Outline each blood parasite and name the species.
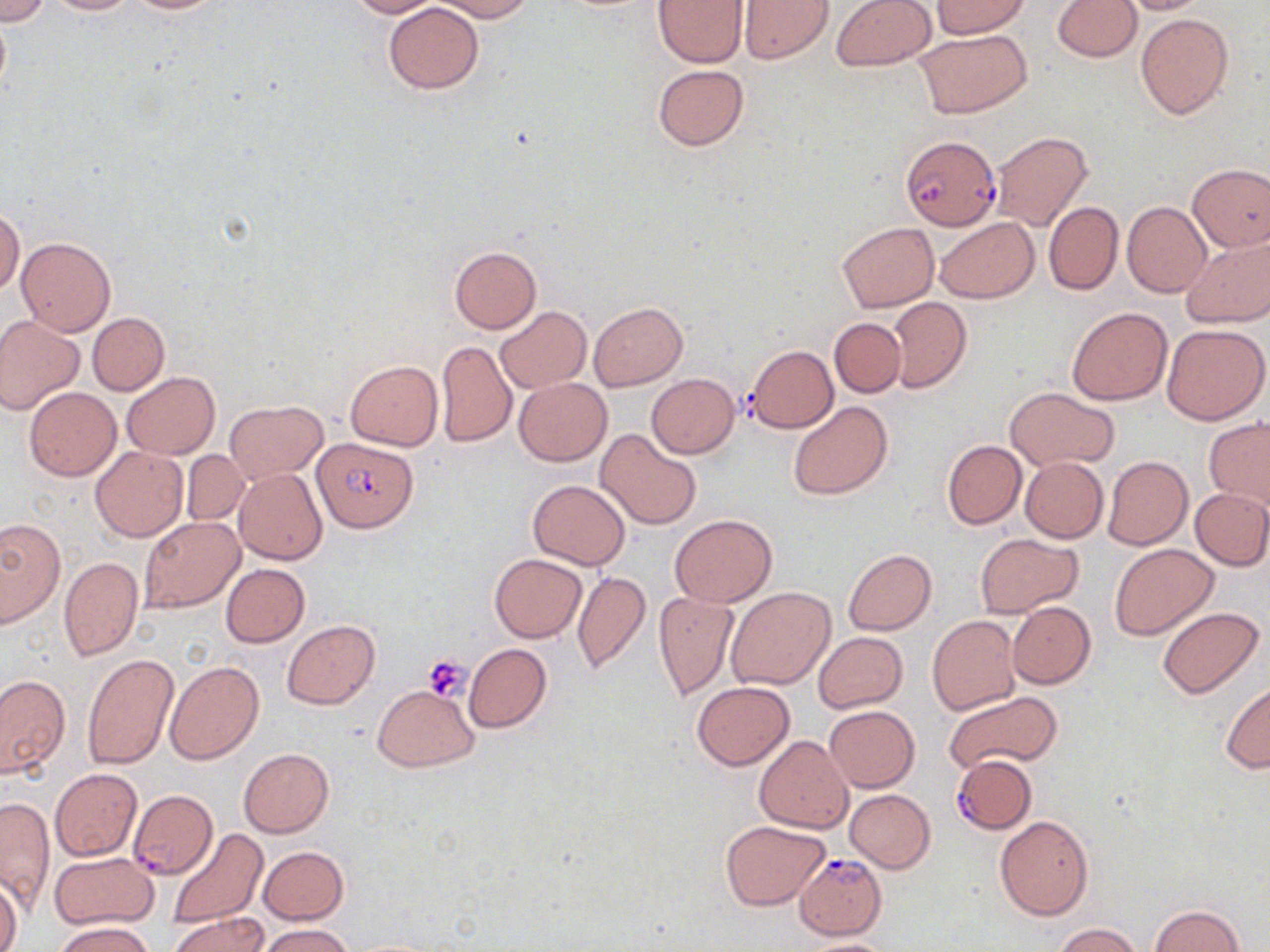
Approximate bounding boxes as named x1/y1/x2/y2 corners in pixels.
Plasmodium falciparum-infected red blood cells: (x1=899, y1=134, x2=998, y2=230), (x1=312, y1=437, x2=416, y2=533), (x1=955, y1=759, x2=1035, y2=837), (x1=128, y1=789, x2=218, y2=879), (x1=794, y1=854, x2=887, y2=940).
No Plasmodium ovale, Plasmodium malariae, Plasmodium vivax, Babesia divergens, or Trypanosoma brucei observed.

Summary:
  - Platelet locations: (x1=422, y1=653, x2=473, y2=702)
  - Uninfected red blood cell locations: (x1=0, y1=0, x2=52, y2=25), (x1=41, y1=0, x2=137, y2=15), (x1=122, y1=0, x2=232, y2=14), (x1=345, y1=0, x2=441, y2=18), (x1=433, y1=0, x2=532, y2=21), (x1=830, y1=0, x2=936, y2=72), (x1=932, y1=0, x2=1028, y2=38), (x1=1053, y1=0, x2=1142, y2=62), (x1=1113, y1=0, x2=1214, y2=15), (x1=653, y1=1, x2=747, y2=67), (x1=739, y1=1, x2=834, y2=64), (x1=383, y1=3, x2=483, y2=93), (x1=0, y1=9, x2=11, y2=103), (x1=1135, y1=12, x2=1234, y2=121), (x1=915, y1=29, x2=1032, y2=118), (x1=653, y1=64, x2=749, y2=151), (x1=991, y1=132, x2=1092, y2=231), (x1=1188, y1=164, x2=1270, y2=251), (x1=1043, y1=202, x2=1123, y2=296), (x1=1121, y1=202, x2=1211, y2=297), (x1=1, y1=207, x2=24, y2=295), (x1=935, y1=216, x2=1038, y2=303), (x1=836, y1=222, x2=938, y2=312), (x1=16, y1=236, x2=115, y2=335), (x1=1181, y1=236, x2=1270, y2=329), (x1=449, y1=246, x2=540, y2=334), (x1=887, y1=297, x2=971, y2=392), (x1=589, y1=302, x2=687, y2=390), (x1=1066, y1=305, x2=1173, y2=406), (x1=495, y1=306, x2=591, y2=393), (x1=88, y1=312, x2=169, y2=395), (x1=0, y1=314, x2=85, y2=415), (x1=829, y1=317, x2=907, y2=397), (x1=1161, y1=323, x2=1269, y2=424), (x1=436, y1=340, x2=517, y2=447), (x1=744, y1=345, x2=838, y2=432), (x1=345, y1=360, x2=442, y2=452), (x1=121, y1=373, x2=218, y2=459), (x1=646, y1=373, x2=740, y2=459), (x1=513, y1=377, x2=612, y2=466), (x1=1006, y1=386, x2=1119, y2=471), (x1=24, y1=387, x2=121, y2=481), (x1=788, y1=400, x2=894, y2=500), (x1=225, y1=401, x2=327, y2=483), (x1=1203, y1=416, x2=1270, y2=512), (x1=596, y1=427, x2=701, y2=530), (x1=941, y1=440, x2=1027, y2=530), (x1=90, y1=447, x2=187, y2=542), (x1=182, y1=451, x2=249, y2=527), (x1=1102, y1=456, x2=1193, y2=550), (x1=1020, y1=457, x2=1109, y2=543), (x1=234, y1=468, x2=328, y2=565), (x1=527, y1=480, x2=630, y2=570), (x1=1190, y1=488, x2=1270, y2=570), (x1=671, y1=514, x2=777, y2=607), (x1=140, y1=517, x2=243, y2=613), (x1=0, y1=519, x2=63, y2=627), (x1=976, y1=532, x2=1080, y2=618), (x1=1109, y1=544, x2=1218, y2=640), (x1=842, y1=549, x2=937, y2=635), (x1=488, y1=553, x2=587, y2=643), (x1=59, y1=556, x2=143, y2=661), (x1=221, y1=563, x2=309, y2=647), (x1=572, y1=570, x2=651, y2=676), (x1=727, y1=588, x2=836, y2=689), (x1=653, y1=590, x2=738, y2=700), (x1=1007, y1=602, x2=1095, y2=688), (x1=1157, y1=607, x2=1263, y2=698), (x1=927, y1=615, x2=1021, y2=716), (x1=282, y1=621, x2=379, y2=708), (x1=813, y1=631, x2=908, y2=713), (x1=464, y1=643, x2=551, y2=732), (x1=82, y1=653, x2=179, y2=769), (x1=166, y1=659, x2=264, y2=763), (x1=0, y1=673, x2=70, y2=779), (x1=691, y1=681, x2=794, y2=770), (x1=1220, y1=681, x2=1269, y2=774), (x1=373, y1=685, x2=477, y2=771), (x1=943, y1=691, x2=1063, y2=771), (x1=824, y1=705, x2=919, y2=793), (x1=753, y1=735, x2=852, y2=833), (x1=238, y1=748, x2=334, y2=837), (x1=50, y1=768, x2=143, y2=861), (x1=846, y1=789, x2=936, y2=873), (x1=1, y1=798, x2=54, y2=913), (x1=994, y1=814, x2=1093, y2=921), (x1=721, y1=819, x2=829, y2=911), (x1=168, y1=828, x2=267, y2=927), (x1=259, y1=846, x2=349, y2=924), (x1=48, y1=852, x2=160, y2=930), (x1=0, y1=877, x2=22, y2=952), (x1=1150, y1=905, x2=1245, y2=952), (x1=171, y1=913, x2=269, y2=952), (x1=51, y1=921, x2=157, y2=952), (x1=1053, y1=923, x2=1145, y2=952), (x1=259, y1=924, x2=353, y2=952), (x1=798, y1=938, x2=901, y2=952)
  - Slide-level diagnosis: Plasmodium falciparum
  - Modality: light microscopy
  - Magnification: 1000x
  - Stain: May-Grünwald-Giemsa
  - Preparation: thin blood film
  - Field of view: single
  - Image size: 1270×952 pixels